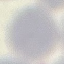 Malaria status: uninfected. Giemsa-stained preparation. Thin blood film. Acquired by smartphone through the microscope eyepiece. Cell patch, automatically extracted from a larger field of view and resized to 64 × 64 pixels.